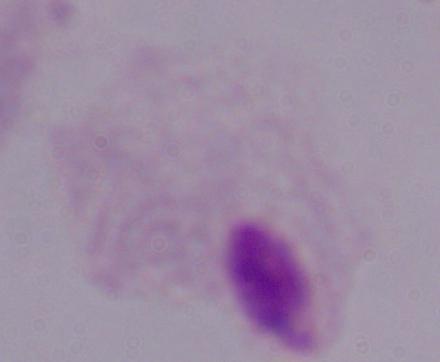
modality = micrograph
identification = trichomonad
magnification = 1000x